Outline each blood parasite and name the species.
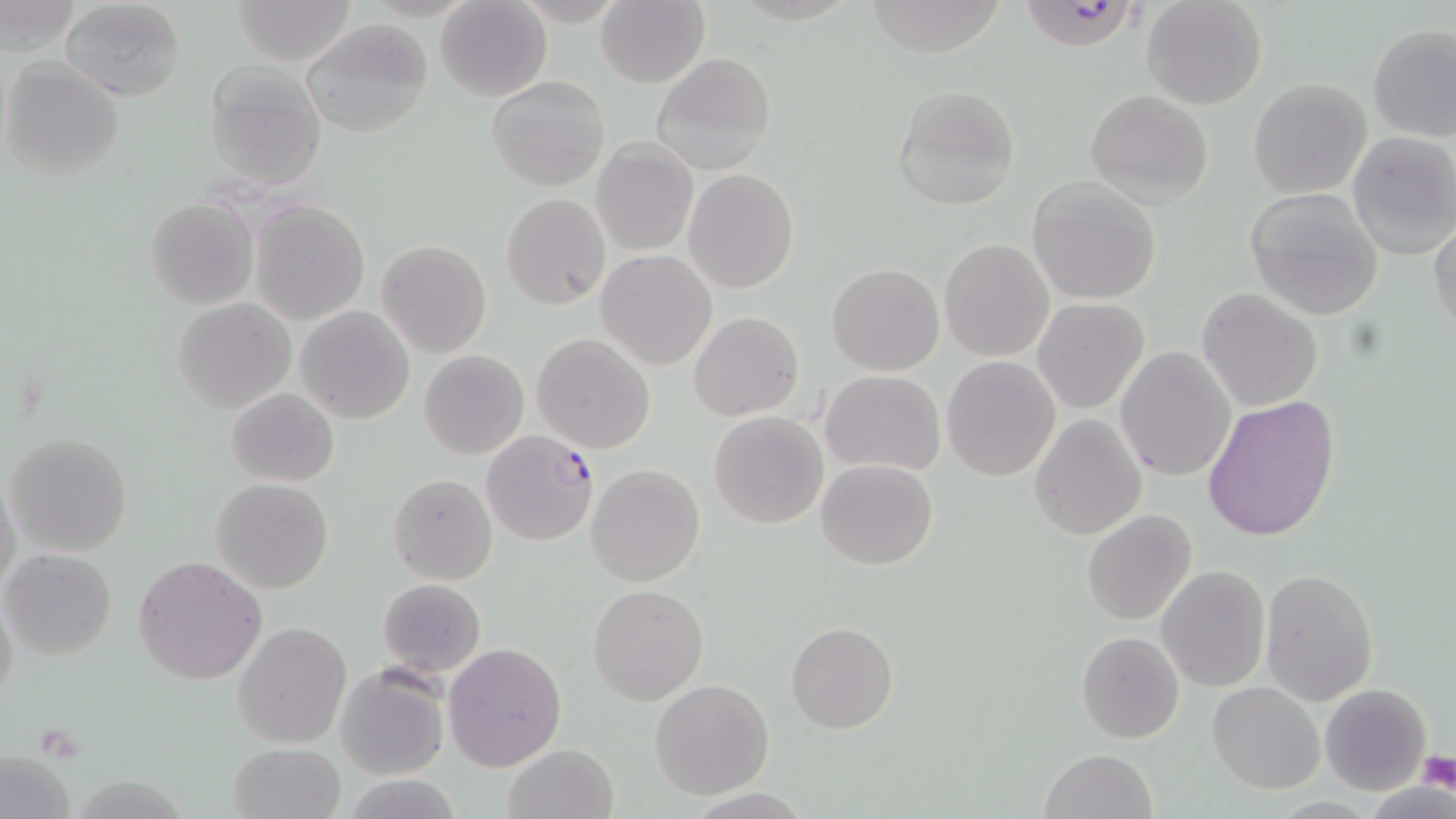
Approximate bounding boxes as (x1, y1, x2, y2) in pixels.
Plasmodium falciparum-infected red blood cells: (1024, 0, 1142, 54).
No Plasmodium ovale, Plasmodium malariae, Plasmodium vivax, Babesia divergens, or Trypanosoma brucei observed.

slide-level diagnosis = Plasmodium falciparum
uninfected red blood cell locations = approximate bounding boxes as (x1, y1, x2, y2) in pixels: (61, 0, 185, 102), (230, 0, 359, 65), (595, 0, 709, 88), (1142, 0, 1268, 111), (1, 1, 80, 57), (436, 1, 552, 101), (866, 1, 1005, 60), (300, 18, 434, 138), (1367, 26, 1456, 144), (652, 53, 776, 175), (3, 58, 125, 179), (203, 62, 327, 190), (486, 74, 611, 191), (1248, 78, 1373, 199), (891, 84, 1021, 211), (1085, 90, 1213, 205), (1347, 133, 1456, 258), (592, 140, 698, 257), (685, 169, 798, 293), (1027, 177, 1162, 305), (1245, 188, 1386, 320), (501, 194, 610, 308), (145, 198, 259, 310), (251, 201, 369, 323), (1429, 218, 1456, 336), (940, 239, 1053, 361), (375, 240, 492, 359), (595, 250, 717, 371), (826, 263, 944, 376), (1197, 287, 1324, 412), (172, 297, 296, 414), (1032, 298, 1149, 414), (296, 307, 414, 423), (688, 312, 804, 422), (531, 333, 655, 455), (1115, 347, 1237, 483), (419, 350, 530, 460), (941, 355, 1061, 481), (820, 370, 946, 474), (227, 387, 339, 487), (1201, 394, 1340, 542), (709, 411, 828, 529), (1028, 414, 1147, 541), (482, 429, 601, 548), (6, 431, 132, 556), (816, 459, 938, 571), (587, 464, 704, 585), (1, 471, 21, 598), (387, 473, 497, 585), (211, 478, 333, 594), (1082, 509, 1197, 625), (2, 549, 116, 660), (135, 554, 267, 684), (1155, 565, 1270, 693), (1259, 569, 1379, 704), (377, 577, 487, 678), (1, 583, 20, 710), (588, 583, 709, 705), (233, 621, 353, 748), (786, 621, 897, 734), (1076, 630, 1185, 743), (443, 641, 567, 772), (334, 666, 449, 780), (650, 679, 773, 799), (1208, 682, 1325, 794), (1320, 683, 1433, 796), (227, 743, 346, 819), (501, 744, 619, 819), (0, 746, 77, 819), (1037, 748, 1159, 819)
modality = optical microscopy
image size = 1456×819 pixels
stain = May-Grünwald-Giemsa
field of view = one of a larger specimen
platelet locations = approximate bounding boxes as (x1, y1, x2, y2) in pixels: (1417, 751, 1456, 793)
preparation = thin blood smear
magnification = 1000x